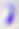
400x magnification. Toxoplasma gondii is seen. Photomicrograph.